Outline each Babesia divergens-infected red blood cell.
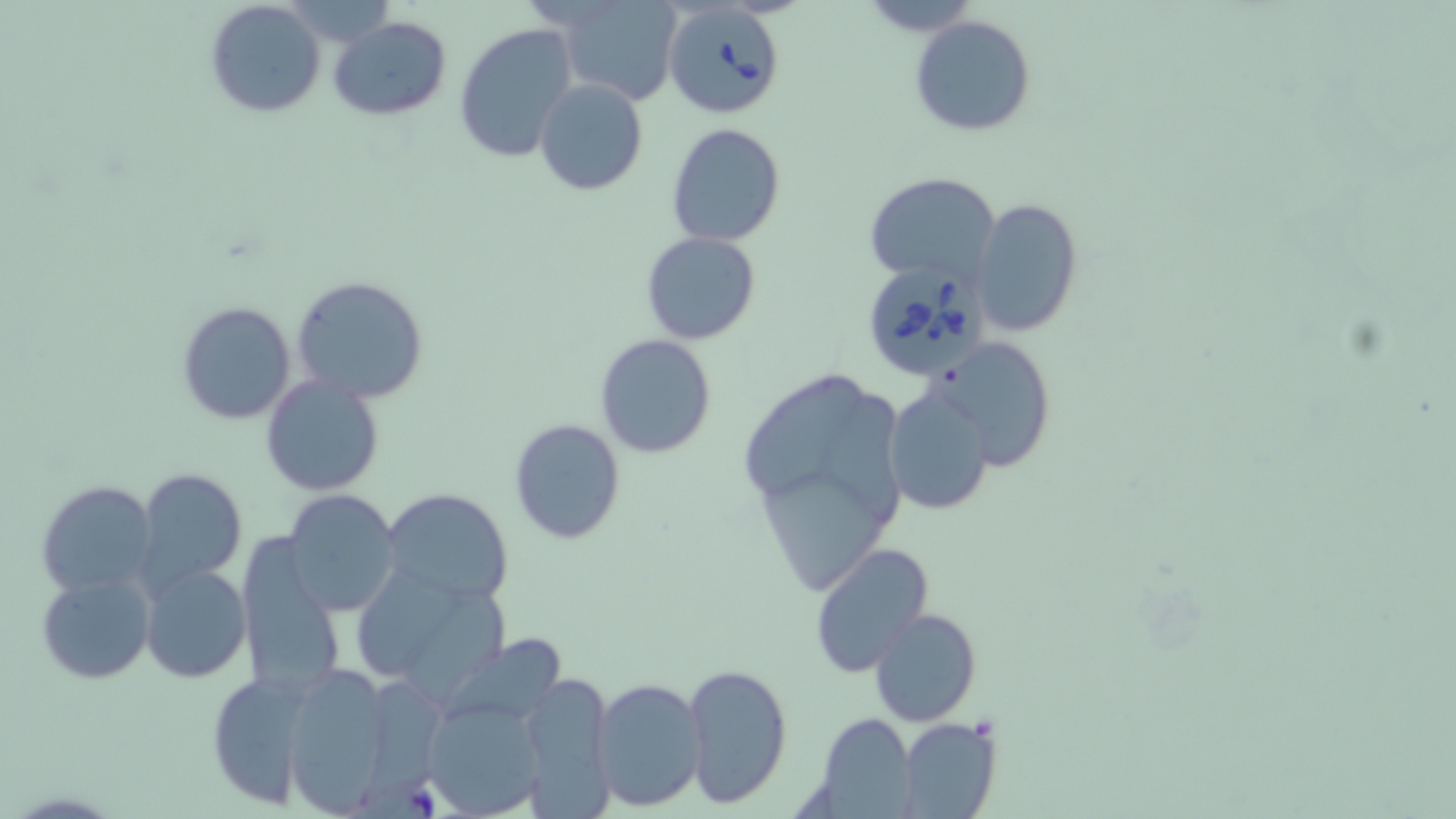

Approximate bounding boxes as (x1,y1)-(x2,y2) corner pairs in pixels.
Babesia divergens-infected red blood cells: (660,0)-(790,118), (860,261)-(989,381).

Uninfected red blood cell locations: (280,0)-(399,51), (204,1)-(327,118), (554,2)-(684,104), (908,14)-(1035,138), (330,16)-(452,121), (453,21)-(579,164), (533,77)-(648,195), (665,122)-(785,247), (864,172)-(1000,285), (971,198)-(1083,338), (641,231)-(762,345), (290,275)-(430,404), (176,301)-(297,426), (930,333)-(1058,469), (594,334)-(717,459), (739,361)-(911,606), (260,375)-(384,496), (885,386)-(993,516), (508,419)-(627,544), (136,468)-(247,591), (34,479)-(159,601), (381,488)-(515,605), (283,489)-(400,617), (235,540)-(346,701), (809,541)-(936,678), (139,563)-(250,683), (349,565)-(509,699), (36,570)-(156,685), (869,608)-(981,727), (440,636)-(580,722), (277,663)-(401,815), (683,663)-(790,805), (518,670)-(615,812), (205,671)-(313,810), (592,677)-(706,811), (421,698)-(548,818), (812,713)-(916,811), (899,718)-(1001,819). Slide-level diagnosis: Babesia divergens. May-Grünwald-Giemsa stain. Image is 1456×819 pixels. Captured at 1000x magnification. One field of a larger specimen. Thin blood film. Optical microscopy.